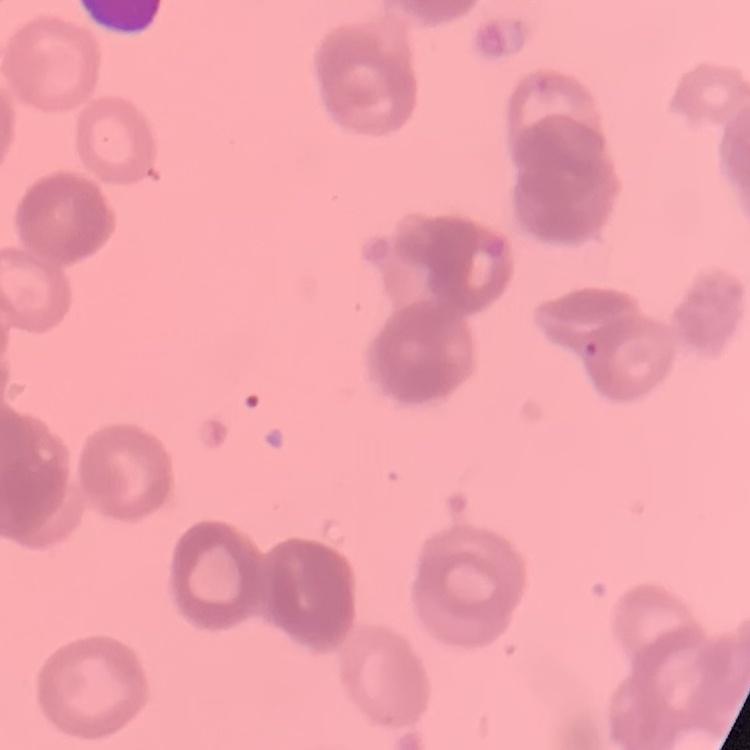

erythrocyte morphology = rouleaux formation
image type = one tile cut from a larger photomicrograph
preparation = thin blood smear
stain = Field's or Giemsa